State the blood parasite species.
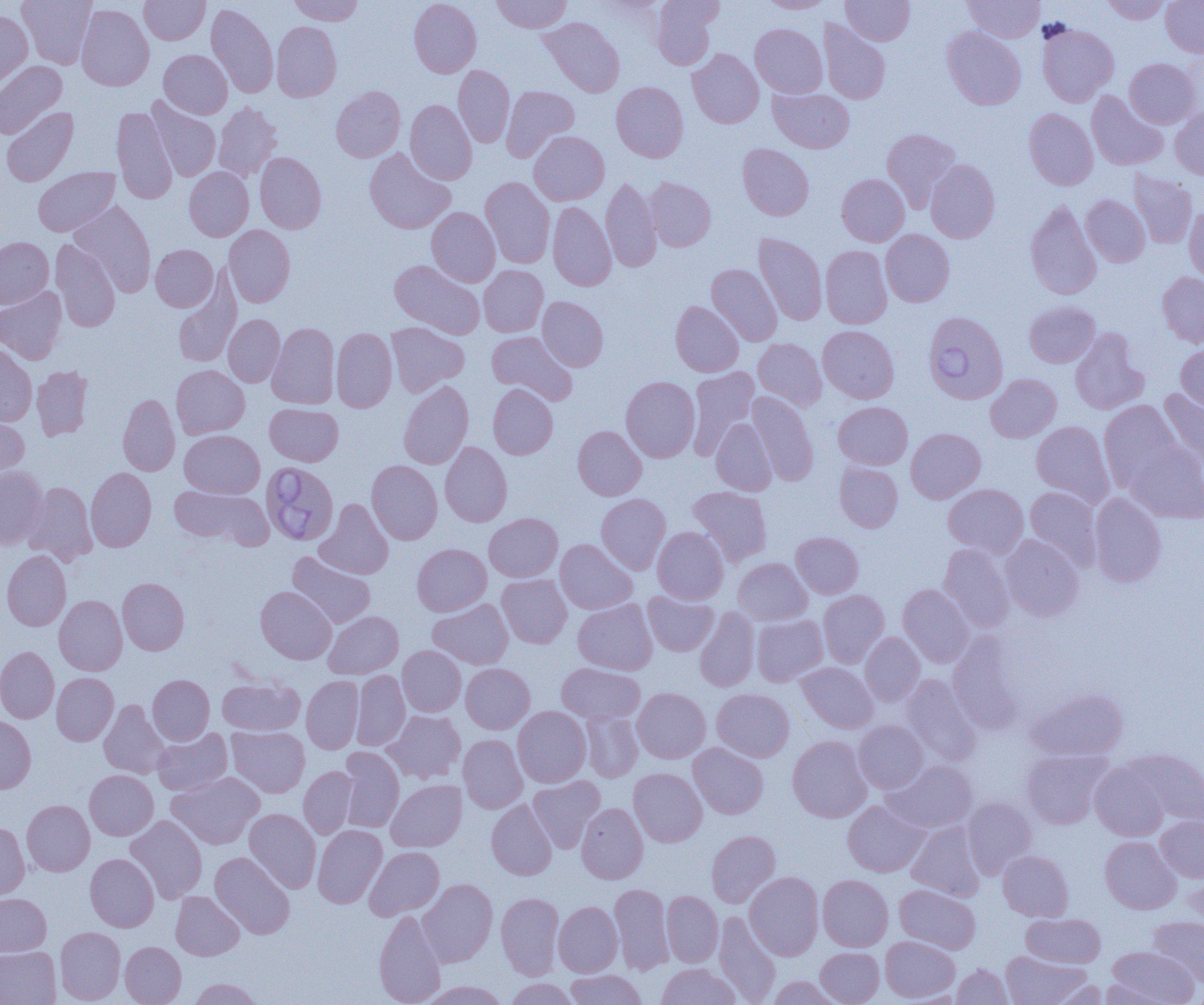
Babesia divergens.

Approximate bounding boxes as (x1, y1, x2, y2) in pixels. Babesia divergens-infected red blood cell locations: (923, 311, 1008, 404), (260, 461, 339, 546). Uninfected red blood cell locations: (17, 0, 97, 68), (139, 0, 210, 45), (289, 0, 364, 26), (409, 0, 481, 77), (492, 0, 571, 33), (650, 0, 721, 70), (759, 0, 833, 13), (840, 0, 914, 45), (964, 0, 1044, 42), (1102, 0, 1170, 24), (1161, 0, 1204, 57), (206, 3, 278, 98), (76, 4, 154, 91), (0, 11, 33, 87), (539, 17, 625, 97), (818, 20, 890, 104), (272, 21, 341, 102), (750, 23, 827, 97), (1037, 23, 1119, 107), (942, 26, 1026, 109), (159, 49, 232, 119), (687, 49, 763, 128), (1124, 58, 1201, 128), (0, 61, 67, 138), (453, 66, 514, 147), (611, 81, 688, 162), (331, 86, 405, 162), (501, 86, 580, 162), (768, 87, 854, 153), (1087, 91, 1168, 170), (146, 97, 220, 181), (405, 100, 476, 184), (214, 102, 282, 181), (111, 106, 177, 204), (1, 107, 78, 187), (1170, 107, 1204, 179), (1024, 108, 1098, 190), (882, 128, 962, 211), (529, 131, 609, 205), (737, 144, 814, 220), (364, 147, 455, 234), (255, 152, 326, 233), (926, 159, 1000, 243), (33, 167, 119, 237), (184, 167, 254, 241), (1129, 172, 1196, 248), (836, 174, 909, 246), (481, 177, 555, 268), (601, 177, 662, 272), (644, 177, 716, 251), (1081, 195, 1150, 267), (1025, 200, 1102, 300), (69, 201, 156, 296), (548, 202, 616, 291), (1184, 205, 1204, 282), (426, 207, 500, 287), (223, 225, 295, 307), (880, 230, 955, 307), (753, 233, 827, 325), (0, 237, 53, 308), (50, 239, 120, 332), (151, 244, 217, 312), (820, 245, 892, 329), (390, 260, 484, 339), (706, 264, 782, 346), (479, 265, 548, 337), (1157, 272, 1204, 347), (173, 278, 241, 368), (0, 286, 66, 364), (537, 296, 608, 371), (670, 301, 744, 376), (1024, 301, 1100, 368), (223, 314, 285, 387), (386, 322, 469, 396), (267, 323, 340, 409), (818, 325, 899, 403), (331, 328, 397, 412), (1070, 328, 1149, 415), (487, 331, 577, 404), (753, 338, 827, 411), (0, 344, 37, 426), (1176, 344, 1204, 413), (32, 365, 93, 441), (171, 365, 249, 439), (686, 366, 760, 456), (986, 374, 1061, 443), (621, 376, 700, 462), (398, 381, 474, 469), (488, 384, 558, 459), (1159, 389, 1204, 466), (747, 391, 819, 486), (118, 393, 180, 475), (1099, 400, 1182, 491), (833, 401, 913, 469), (265, 403, 343, 466), (0, 414, 29, 480), (711, 418, 777, 496), (1031, 421, 1115, 507), (573, 426, 646, 500), (906, 428, 986, 503), (179, 430, 265, 498), (1124, 441, 1204, 523), (440, 442, 512, 527), (366, 460, 443, 544), (834, 462, 903, 532), (0, 465, 48, 549), (85, 467, 156, 552), (23, 482, 97, 566), (944, 483, 1028, 558), (169, 485, 270, 548), (686, 486, 772, 567), (1025, 486, 1103, 569), (596, 493, 671, 574), (1089, 493, 1166, 587), (316, 499, 393, 579), (484, 513, 563, 582), (652, 526, 729, 604), (791, 532, 863, 598), (1000, 534, 1084, 621), (555, 539, 637, 614), (412, 543, 491, 615), (938, 543, 1015, 632), (2, 550, 71, 631), (287, 551, 375, 628), (733, 558, 812, 625), (497, 574, 572, 648), (117, 577, 189, 655), (898, 584, 974, 667), (255, 586, 336, 664), (818, 590, 889, 667), (642, 592, 718, 656), (54, 595, 127, 675), (428, 598, 513, 669), (573, 599, 657, 674), (694, 607, 760, 692), (323, 611, 403, 678), (752, 615, 828, 686), (860, 632, 925, 706), (948, 632, 1024, 733), (397, 646, 466, 716), (0, 647, 59, 723), (796, 662, 878, 733), (461, 663, 535, 734), (556, 663, 645, 724), (351, 670, 410, 751), (52, 672, 118, 745), (147, 674, 215, 744), (901, 674, 981, 765), (217, 675, 304, 735), (301, 676, 364, 754), (1027, 687, 1129, 761), (632, 688, 710, 763), (712, 688, 794, 762), (99, 700, 170, 778), (512, 706, 591, 787), (581, 709, 642, 782), (383, 710, 465, 783), (0, 716, 36, 793), (854, 720, 928, 793), (227, 726, 309, 797), (152, 728, 232, 796), (459, 734, 527, 812), (787, 735, 872, 822), (689, 743, 768, 819), (339, 747, 404, 832), (1021, 749, 1112, 829), (1131, 749, 1204, 826), (1090, 759, 1171, 840), (884, 760, 978, 833), (299, 766, 357, 838), (629, 768, 707, 847), (84, 770, 158, 840), (167, 772, 264, 849), (528, 776, 605, 852), (386, 779, 466, 852), (962, 797, 1036, 879), (486, 799, 557, 880), (22, 800, 95, 876), (843, 800, 928, 876), (576, 803, 648, 883), (244, 808, 321, 893), (126, 815, 207, 903), (1156, 815, 1204, 882), (0, 821, 30, 899), (907, 821, 986, 901), (313, 825, 387, 908), (706, 830, 780, 907), (1100, 836, 1181, 914), (364, 846, 444, 920), (998, 850, 1074, 921), (210, 852, 295, 939), (85, 854, 159, 931), (1184, 866, 1204, 928), (745, 872, 823, 960), (818, 875, 893, 951), (418, 879, 497, 967), (609, 883, 673, 974), (894, 884, 981, 953), (170, 891, 244, 960), (661, 891, 723, 967), (0, 892, 51, 957), (496, 893, 563, 979), (554, 901, 622, 977), (373, 909, 447, 1005), (714, 912, 781, 1004), (1021, 913, 1105, 967), (1147, 916, 1204, 986), (54, 927, 125, 1004), (880, 935, 960, 1002), (120, 941, 186, 1005), (0, 947, 61, 1005), (815, 947, 884, 1005), (1107, 947, 1198, 1004), (1001, 950, 1090, 1005), (656, 963, 741, 1005), (953, 964, 1012, 1004), (565, 969, 646, 1004), (766, 976, 841, 1005), (189, 978, 263, 1005), (504, 978, 579, 1005), (1048, 979, 1107, 1005), (1099, 979, 1173, 1004), (418, 981, 510, 1005). Thin blood smear. Image is 1204×1005 pixels. One field of a larger specimen. Light microscopy. 1000x magnification.